Comment on the morphology of the red blood cells.
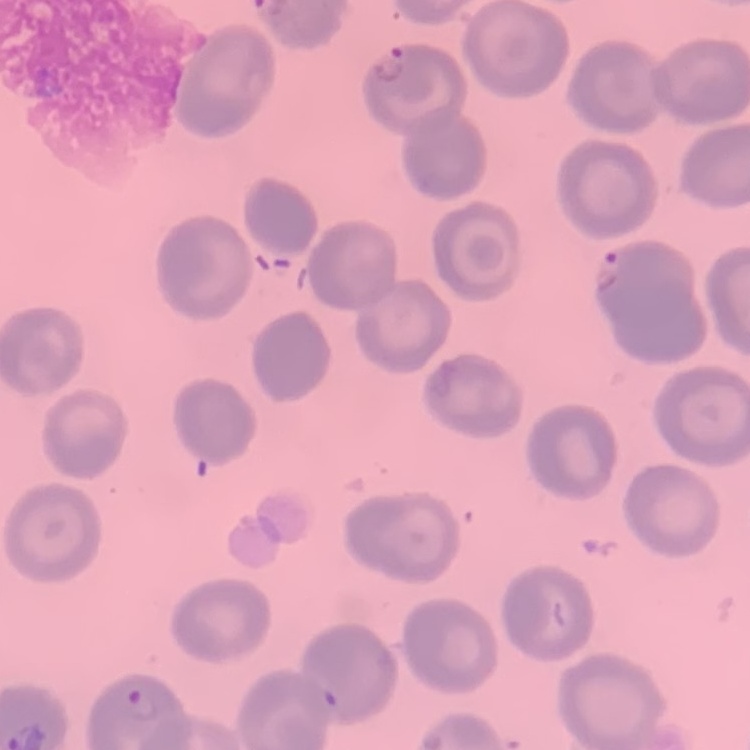
They show no rouleaux formation.

Summary:
  - Image type: one tile cut from a larger photomicrograph
  - Preparation: thin peripheral smear
  - Stain: Field's or Giemsa